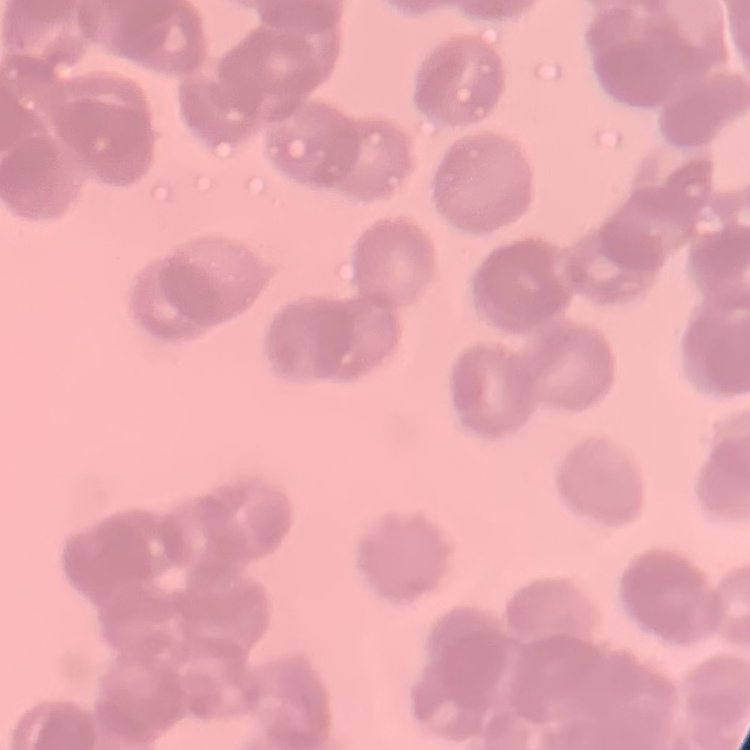

Summary:
  - Red blood cell morphology: rouleaux formation
  - Preparation: thin peripheral smear
  - Stain: Field's or Giemsa
  - Image type: one tile cut from a larger photomicrograph